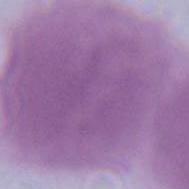
modality = photomicrograph
identification = red blood cell
magnification = 1000x